Report the malaria status of this cell.
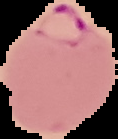
It is parasitized.

image type = segmented cell region with the area outside set to black
image size = 118×139 pixels
preparation = thin blood film